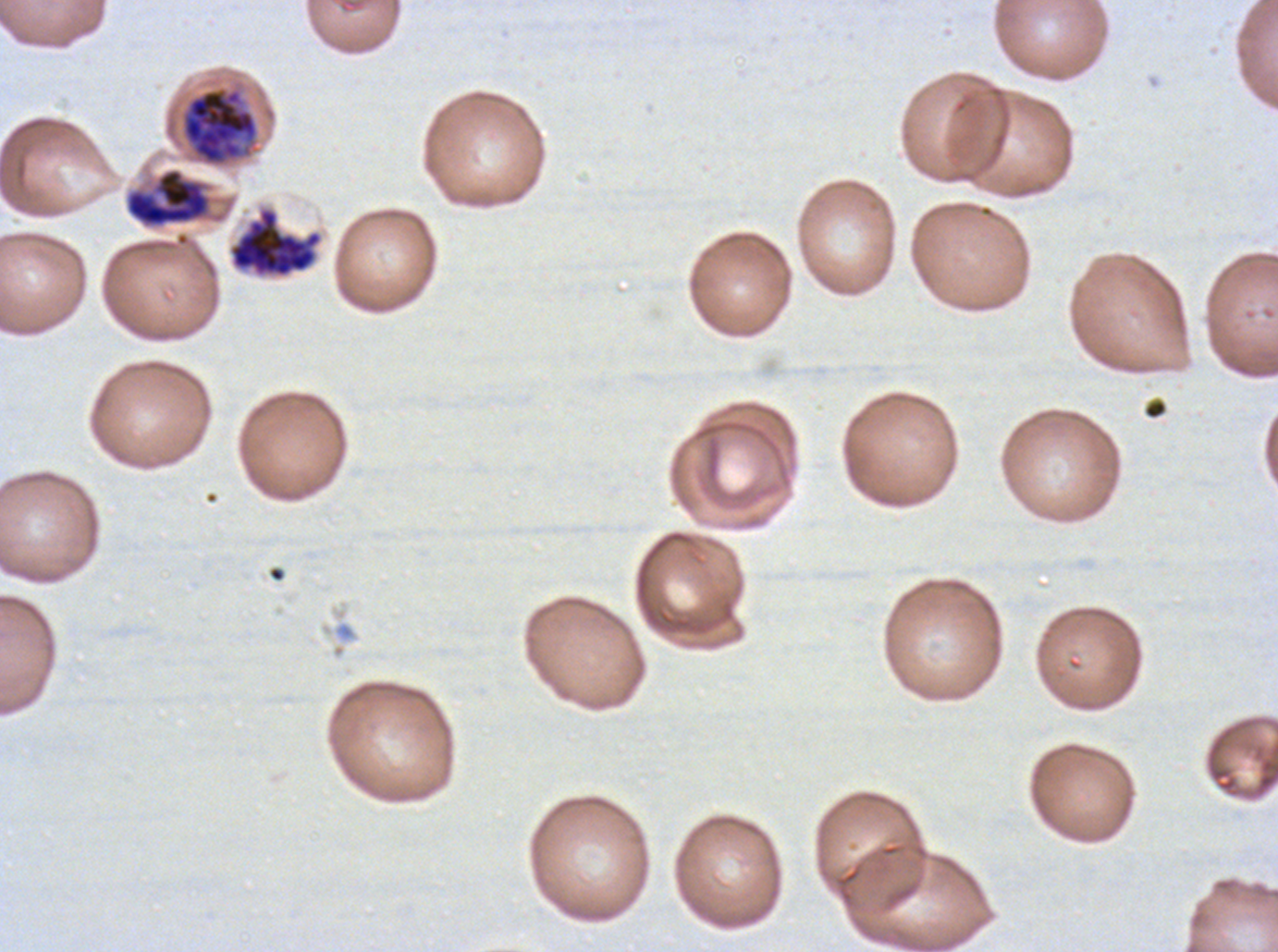
Approximate bounding boxes as (x1, y1, x2, y2) in pixels.
Summary:
  - Late schizont locations: (181, 86, 259, 165), (228, 207, 323, 278)
  - Late trophozoite locations: (125, 168, 211, 227)
  - Life-cycle stages observed: late trophozoite, late schizont
  - Preparation: thin blood film
  - Stain: Giemsa
  - Field of view: sub-image separated from a larger composite
  - Image size: 1278×952 pixels
  - Specimen: P. falciparum from a patient in The Gambia, cultured ex vivo for 24 to 48 hours